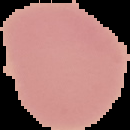 Image is 130×130 pixels. The area outside the segmented cell region is set to black. From a thin blood smear. Result: no malaria parasites seen.